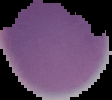
Summary:
  - Image size: 112×100 pixels
  - Preparation: thin blood smear
  - Malaria status: uninfected
  - Image type: segmented cell region with the area outside set to black